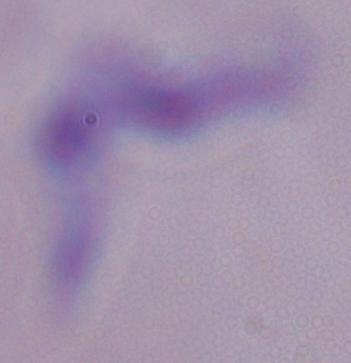
identification: trypanosome
magnification: 1000x
modality: micrograph